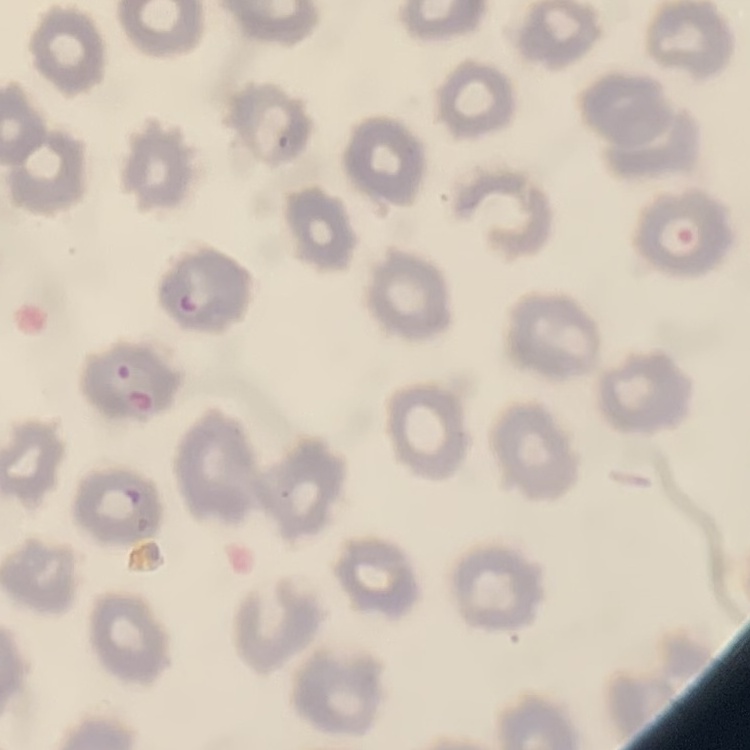

{
  "erythrocyte_morphology": "no rouleaux formation",
  "stain": "Field's or Giemsa",
  "image_type": "one tile cut from a larger photomicrograph",
  "preparation": "thin blood film"
}